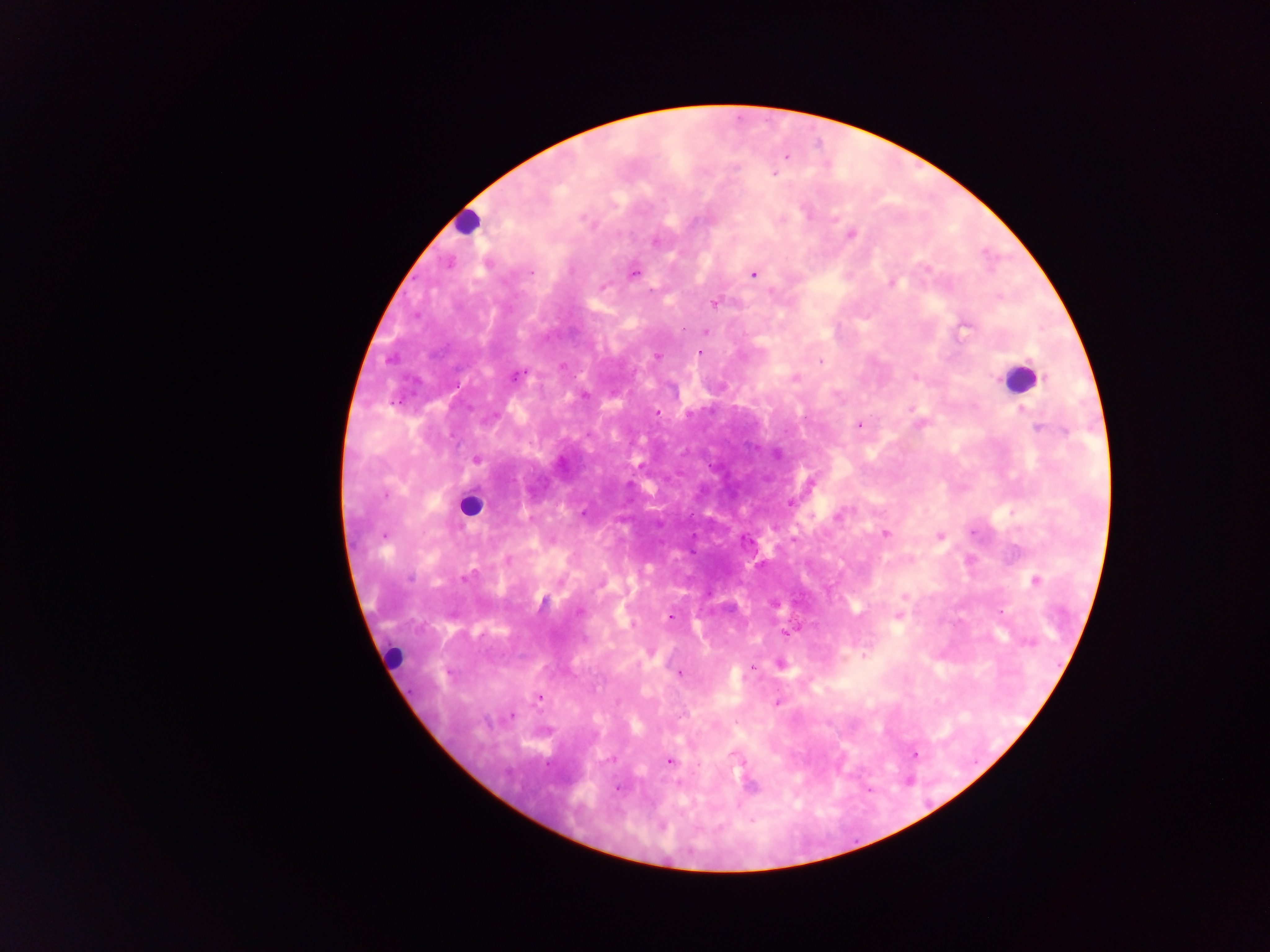

Approximate centers as [x, y] in pixels.
Summary:
  - Leukocyte locations: [465, 222], [1018, 377], [470, 505], [393, 657]
  - Malaria parasite locations: [786, 157], [774, 173], [805, 212], [782, 220], [851, 234], [655, 241], [926, 269], [532, 271], [633, 274], [752, 274], [892, 284], [602, 286], [715, 304], [964, 327], [706, 331], [700, 353], [657, 356], [821, 362], [562, 366], [517, 376], [915, 377], [795, 379], [912, 409], [1021, 411], [658, 413], [859, 425], [1037, 429], [476, 460], [790, 503], [582, 513], [838, 516], [973, 532], [886, 533], [384, 536], [940, 537], [508, 561], [410, 579], [463, 579], [1034, 580], [904, 597], [580, 611], [1001, 612], [899, 615], [671, 617], [786, 633], [864, 655], [781, 664], [753, 667], [680, 674], [539, 697], [777, 703], [512, 715], [915, 754], [734, 755], [611, 760], [670, 761], [750, 785], [618, 789]
  - Field of view: single
  - Capture: mobile-phone photograph through a microscope
  - Preparation: thick blood smear
  - Country: Ghana
  - Image size: 1270×952 pixels